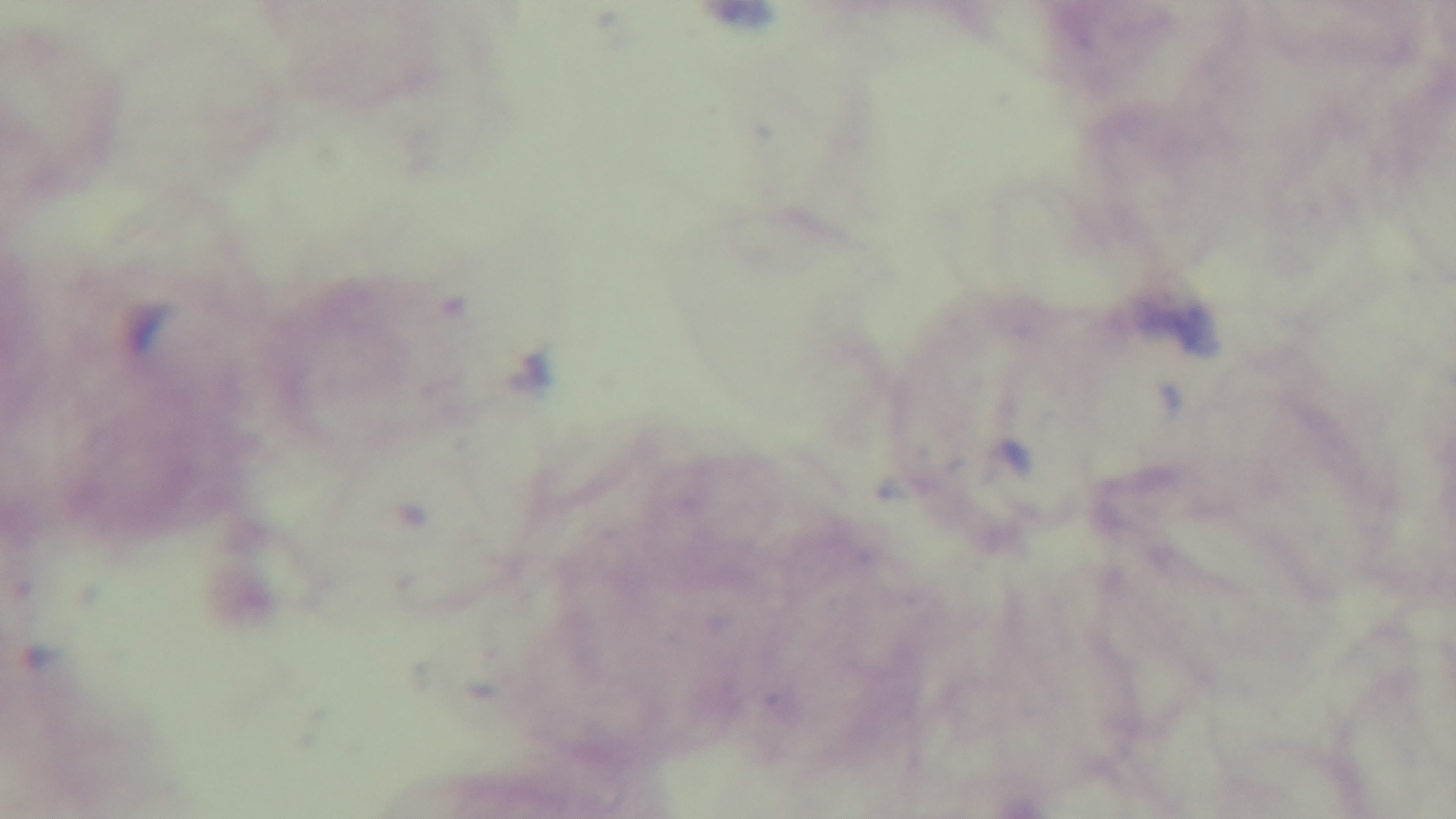
objective = 100x oil immersion
capture = mounted 4K digital camera
malaria status = uninfected
preparation = thick blood film
field of view = one from the slide
stain = Giemsa
modality = light microscopy